Assess this cell for malaria.
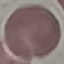
It is uninfected.

Photographed with a smartphone camera at the microscope eyepiece. Automatically extracted cell patch, resized to 64 × 64 pixels. Thin blood film. Giemsa-stained preparation.